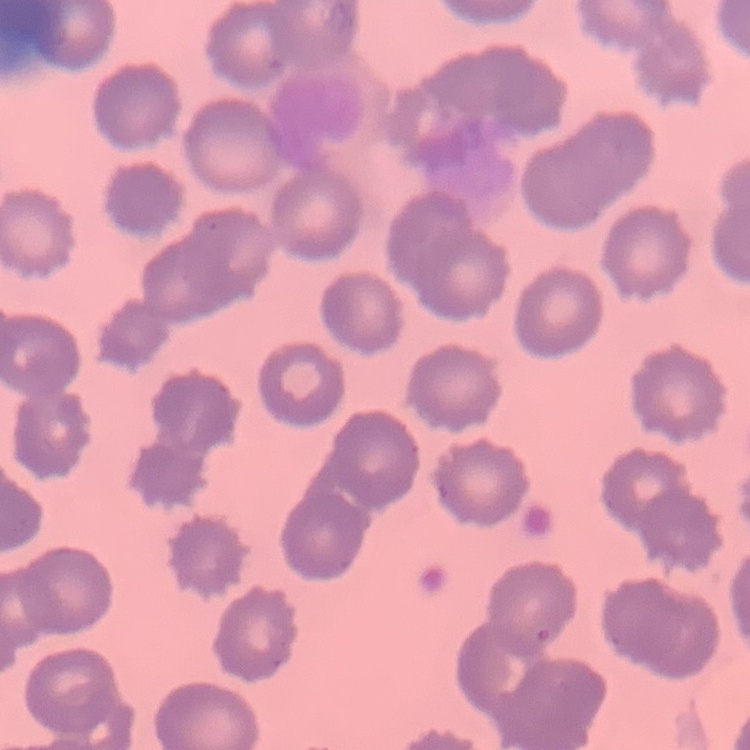 The red blood cells show no rouleaux formation. Field's or Giemsa stain. Thin blood film. One tile cut from a larger photomicrograph.